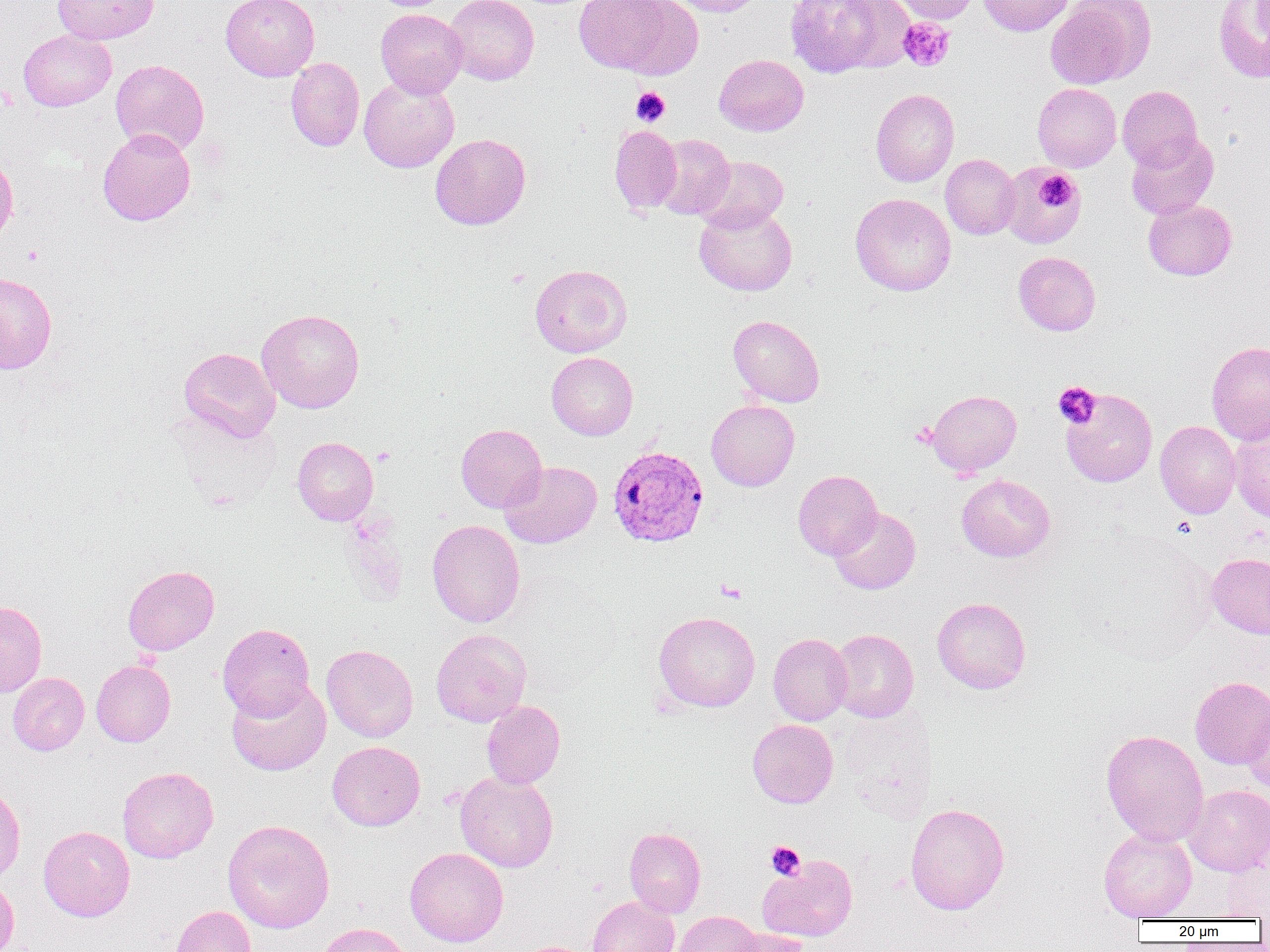
Approximate bounding boxes as (x1,y1)-(x2,y2) corner pairs in pixels. Uninfected red blood cell locations: (52,0)-(158,44), (220,0)-(320,81), (445,0)-(539,85), (573,0)-(700,78), (666,0)-(764,17), (783,0)-(909,78), (889,0)-(982,23), (979,0)-(1076,36), (1045,0)-(1155,90), (1213,0)-(1270,83), (375,9)-(468,97), (19,30)-(116,111), (714,54)-(808,136), (286,57)-(365,151), (110,59)-(209,155), (359,76)-(459,173), (1032,83)-(1121,172), (1117,85)-(1201,170), (870,88)-(959,187), (609,125)-(682,214), (97,128)-(196,226), (1126,131)-(1219,219), (430,133)-(531,230), (652,134)-(735,219), (940,154)-(1021,239), (0,155)-(18,244), (696,155)-(789,233), (999,162)-(1085,249), (850,193)-(956,296), (1143,198)-(1236,280), (694,204)-(797,296), (1013,251)-(1101,335), (530,264)-(632,357), (0,272)-(57,374), (257,308)-(364,413), (728,315)-(825,407), (1206,341)-(1270,444), (179,347)-(280,442), (546,352)-(638,440), (1060,388)-(1157,487), (926,390)-(1022,478), (706,400)-(799,491), (1155,420)-(1241,519), (1229,420)-(1270,523), (456,424)-(547,513), (292,437)-(378,525), (500,461)-(602,548), (792,470)-(882,559), (957,474)-(1055,562), (829,507)-(921,594), (426,519)-(525,627), (1207,553)-(1270,639), (122,565)-(219,655), (932,596)-(1031,694), (0,600)-(47,698), (653,611)-(760,712), (217,623)-(315,719), (432,629)-(531,727), (830,629)-(918,722), (768,633)-(852,725), (322,644)-(418,742), (91,659)-(176,747), (7,672)-(89,756), (1190,676)-(1270,769), (227,680)-(331,776), (1242,698)-(1270,794), (481,701)-(565,788), (747,719)-(838,808), (1101,729)-(1209,846), (327,741)-(425,831), (117,766)-(219,863), (455,771)-(558,872), (0,781)-(26,886), (1184,784)-(1270,876), (905,803)-(1009,915), (222,819)-(335,933), (38,825)-(134,921), (624,826)-(706,918), (1099,828)-(1197,921), (405,847)-(508,947), (1221,854)-(1270,919), (757,855)-(857,942), (0,878)-(19,951), (587,896)-(679,952), (169,905)-(257,952), (672,911)-(762,952), (311,922)-(411,952), (726,928)-(811,952). Plasmodium vivax-infected red blood cell locations: (608,444)-(709,549). Platelet locations: (898,18)-(955,72), (631,87)-(670,126), (1038,172)-(1075,210), (23,246)-(44,266), (1053,381)-(1101,429), (911,423)-(937,447), (373,447)-(396,466), (716,579)-(746,603), (765,841)-(806,879). Slide-level diagnosis: Plasmodium vivax. Image is 1270×952 pixels. Optical microscopy. Thin blood smear. Captured at 1000x magnification. One field of a larger specimen.